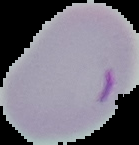
image size = 139×145 pixels
preparation = thin blood smear
malaria status = parasitized
image type = cell region segmented out of the field of view; surrounding area masked to black